Give the extent of all Trypanosoma brucei.
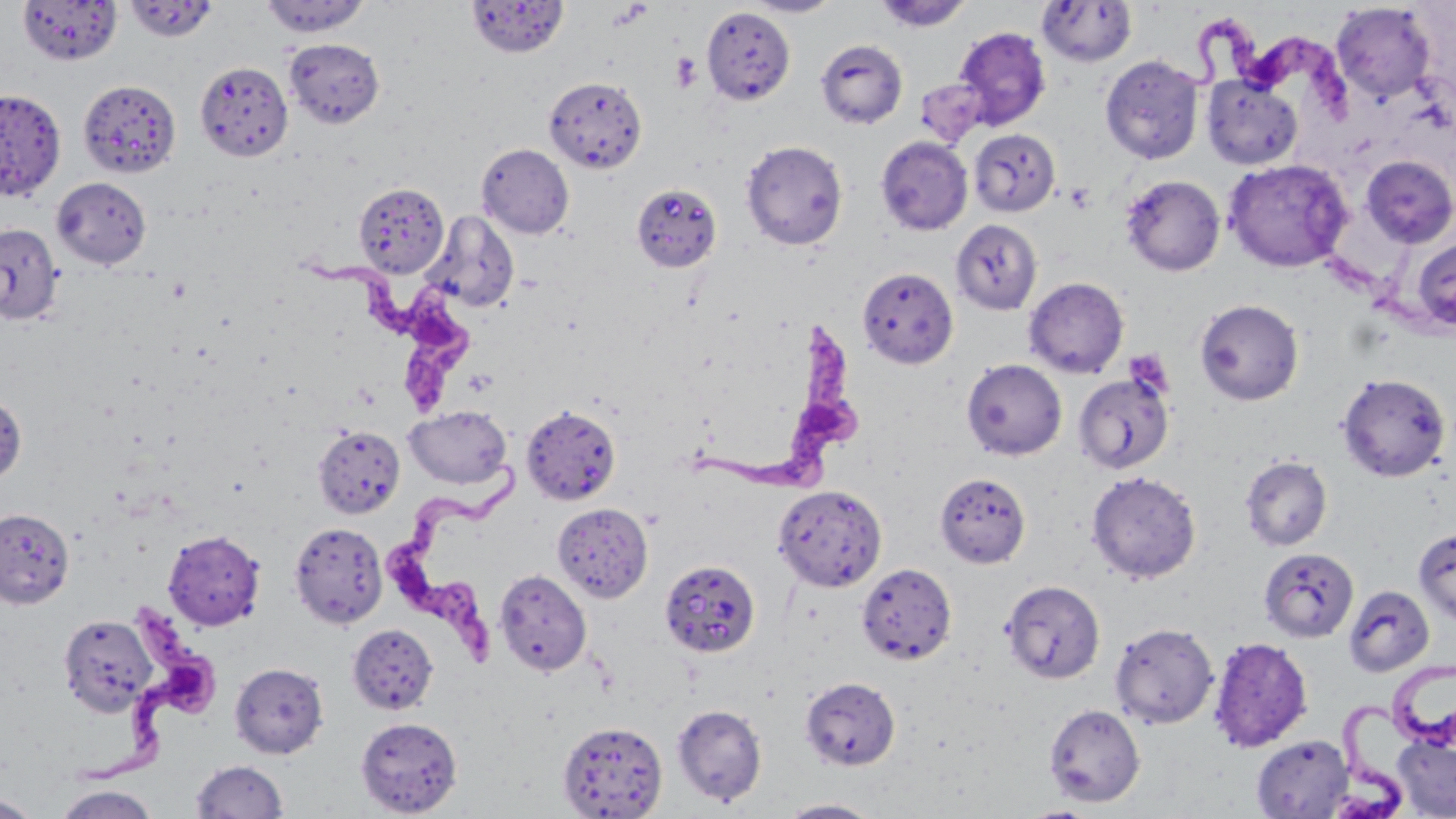
Approximate bounding boxes as (x1, y1, x2, y2) in pixels.
Trypanosoma brucei: (1177, 9, 1359, 127), (312, 251, 483, 420), (677, 320, 865, 511), (387, 451, 538, 672), (83, 603, 236, 786), (1385, 655, 1456, 751), (1329, 702, 1420, 817).

Summary:
  - Platelet locations: (671, 53, 702, 92), (1064, 183, 1095, 213)
  - Uninfected red blood cell locations: (18, 0, 122, 65), (260, 0, 370, 37), (466, 0, 569, 58), (743, 0, 843, 17), (874, 0, 973, 32), (123, 1, 219, 42), (1037, 1, 1137, 67), (1331, 3, 1436, 102), (702, 6, 796, 106), (954, 26, 1051, 129), (284, 38, 384, 128), (816, 39, 907, 129), (1100, 54, 1204, 164), (195, 60, 293, 160), (1202, 74, 1303, 169), (544, 75, 647, 174), (916, 77, 990, 147), (78, 79, 181, 178), (0, 88, 66, 200), (969, 129, 1060, 217), (876, 136, 973, 236), (741, 140, 848, 250), (477, 143, 574, 239), (1360, 156, 1455, 248), (1223, 158, 1353, 272), (1121, 174, 1225, 276), (52, 177, 151, 269), (355, 182, 449, 277), (625, 184, 725, 275), (422, 211, 519, 312), (951, 219, 1042, 314), (0, 223, 63, 325), (1410, 237, 1456, 333), (857, 267, 958, 368), (1024, 277, 1128, 378), (1195, 298, 1304, 406), (961, 359, 1067, 460), (1073, 373, 1174, 476), (1336, 373, 1451, 482), (0, 393, 27, 484), (521, 404, 621, 505), (403, 405, 513, 490), (312, 426, 406, 519), (1240, 455, 1332, 551), (1086, 470, 1201, 583), (935, 472, 1031, 568), (773, 484, 887, 592), (553, 503, 653, 602), (0, 508, 74, 608), (289, 521, 388, 629), (1414, 527, 1456, 626), (163, 530, 266, 631), (1259, 547, 1358, 642), (660, 560, 761, 658), (856, 562, 957, 665), (494, 568, 592, 676), (1001, 579, 1106, 684), (1343, 584, 1435, 677), (57, 614, 158, 716), (1110, 622, 1219, 729), (347, 624, 439, 715), (1208, 637, 1313, 752), (229, 661, 329, 759), (800, 676, 901, 771), (671, 704, 768, 807), (1044, 704, 1145, 807), (355, 716, 463, 817), (557, 720, 668, 818), (1392, 734, 1456, 817), (1252, 735, 1353, 818), (191, 759, 289, 818), (53, 784, 160, 819), (0, 794, 42, 818), (775, 798, 885, 817)
  - Slide-level diagnosis: Trypanosoma brucei
  - Stain: May-Grünwald-Giemsa
  - Magnification: 1000x
  - Preparation: thin blood smear
  - Modality: optical microscopy
  - Image size: 1456×819 pixels
  - Field of view: single